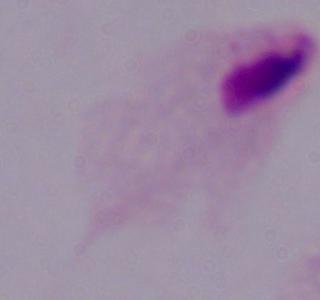

Summary:
  - Modality: photomicrograph
  - Magnification: 1000x
  - Identification: trichomonad